Assess this cell for malaria.
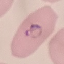

It is parasitized.

Thin blood film. Cell patch, automatically extracted from a larger field of view and resized to 64 × 64 pixels. Giemsa stain. Photographed with a smartphone camera at the microscope eyepiece.